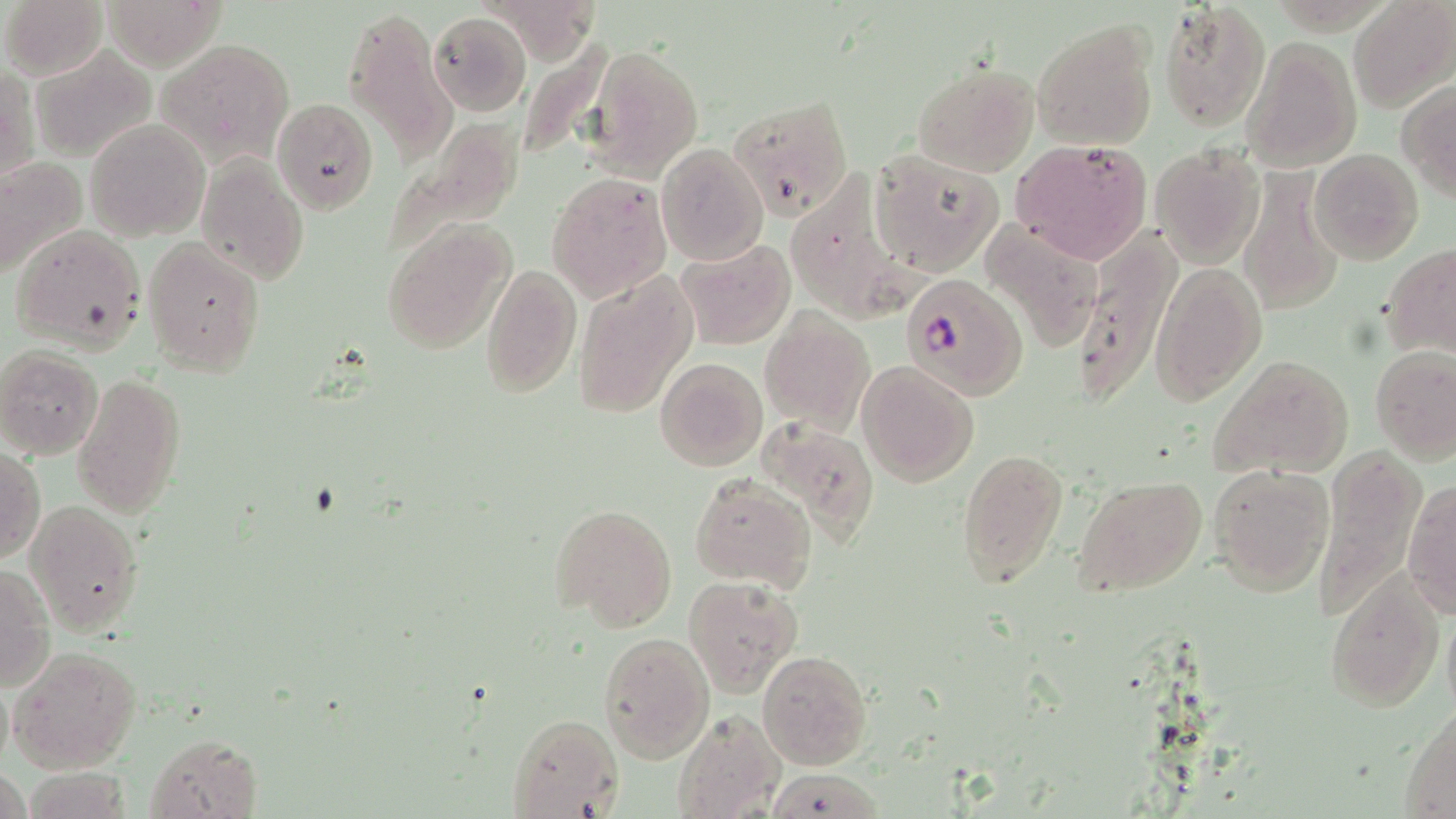
Summary:
  - Coordinate format: approximate bounding boxes as (x1, y1, x2, y2) in pixels
  - Plasmodium falciparum-infected red blood cell locations: (900, 272, 1029, 399)
  - Uninfected red blood cell locations: (3, 0, 109, 80), (103, 0, 228, 69), (476, 0, 604, 67), (1157, 0, 1272, 133), (1349, 0, 1456, 113), (342, 3, 460, 160), (428, 12, 532, 116), (1032, 19, 1159, 151), (1242, 36, 1362, 171), (157, 37, 297, 167), (584, 43, 704, 180), (31, 47, 156, 161), (912, 63, 1039, 177), (1, 68, 38, 184), (1397, 78, 1456, 199), (272, 97, 380, 214), (728, 97, 854, 220), (86, 119, 211, 242), (376, 119, 525, 262), (1011, 139, 1154, 263), (656, 143, 768, 265), (1150, 143, 1266, 267), (1308, 148, 1423, 265), (869, 150, 1003, 276), (196, 154, 310, 286), (0, 156, 87, 284), (782, 171, 938, 330), (1238, 171, 1344, 317), (547, 173, 673, 302), (381, 217, 515, 356), (979, 217, 1104, 353), (11, 223, 149, 352), (1070, 223, 1181, 402), (142, 237, 267, 377), (675, 237, 796, 350), (1380, 244, 1455, 359), (481, 261, 582, 396), (1150, 262, 1266, 404), (572, 269, 698, 422), (761, 305, 873, 437), (1370, 345, 1456, 463), (0, 347, 105, 459), (1208, 353, 1355, 481), (654, 357, 768, 472), (857, 360, 979, 486), (72, 372, 187, 519), (755, 415, 881, 545), (0, 446, 45, 566), (956, 447, 1068, 591), (1316, 448, 1425, 621), (1208, 462, 1333, 596), (687, 473, 816, 593), (1072, 474, 1208, 599), (1401, 479, 1455, 618), (25, 500, 144, 636), (549, 502, 679, 632), (1, 563, 54, 693), (1323, 569, 1444, 712), (684, 576, 803, 697), (1442, 611, 1456, 719), (599, 633, 714, 762), (10, 645, 141, 773), (758, 650, 873, 771), (1, 674, 13, 775), (1400, 706, 1456, 817), (673, 709, 785, 819), (508, 713, 623, 818), (145, 733, 263, 818), (1, 762, 28, 819), (762, 767, 883, 817), (20, 769, 136, 815)
  - Slide-level diagnosis: Plasmodium falciparum
  - Magnification: 1000x
  - Modality: light microscopy
  - Stain: May-Grünwald-Giemsa
  - Field of view: one of a larger specimen
  - Image size: 1456×819 pixels
  - Preparation: thin blood film